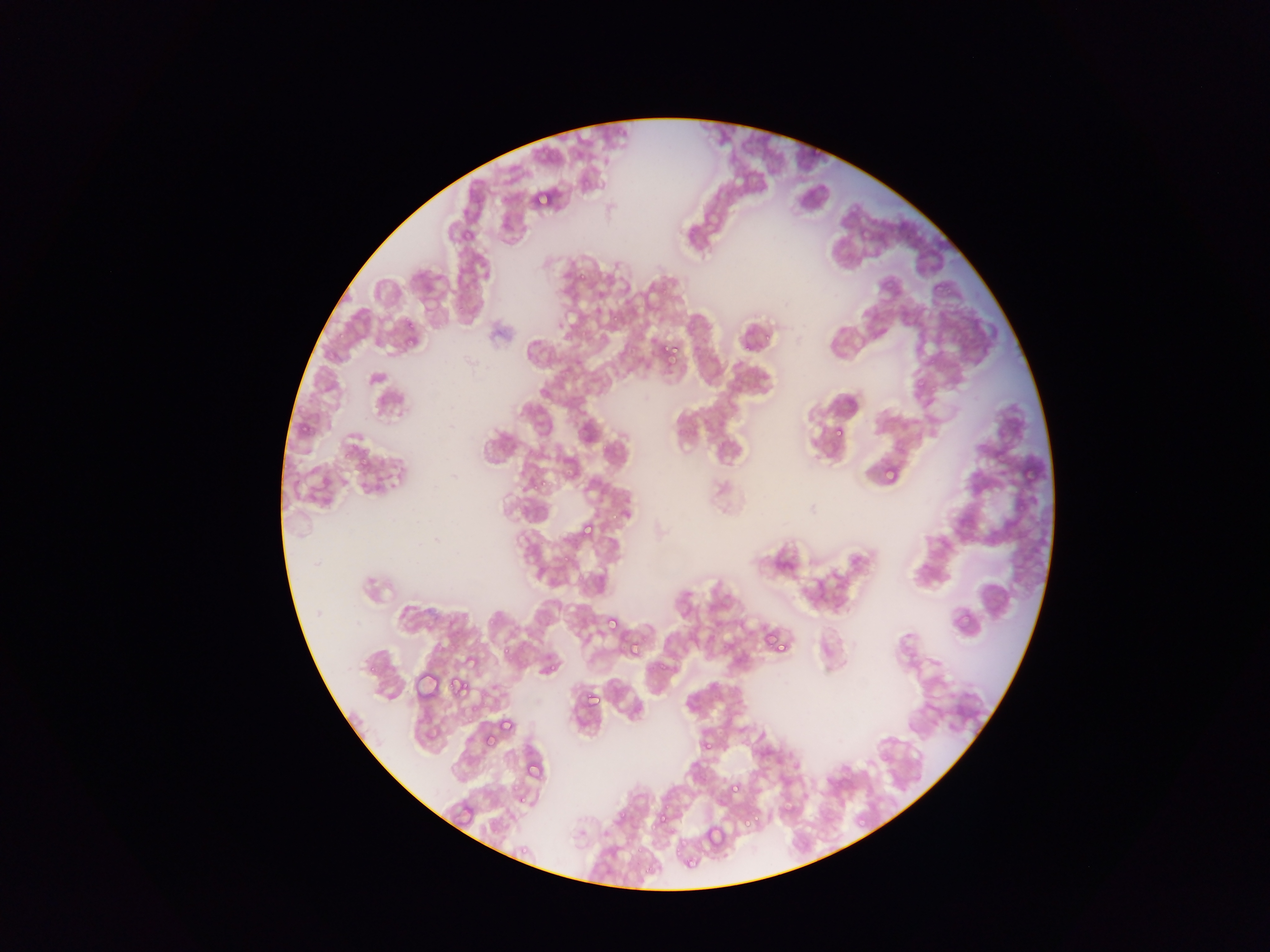

Approximate bounding boxes as [left, top, right, bottom] in pixels.
Summary:
  - Plasmodium parasite locations: [533, 186, 554, 204], [933, 282, 943, 292], [899, 307, 909, 318], [404, 320, 414, 331], [335, 330, 344, 340], [660, 343, 676, 359], [926, 354, 938, 366], [914, 377, 926, 391], [296, 422, 315, 439], [833, 425, 844, 436], [996, 438, 1011, 454], [993, 446, 1009, 462], [1020, 463, 1035, 479], [882, 464, 899, 483], [539, 474, 557, 489], [601, 507, 621, 524], [579, 522, 596, 540], [559, 552, 576, 566], [952, 609, 972, 630], [605, 615, 620, 630], [765, 628, 784, 649], [761, 629, 776, 646], [494, 634, 516, 657], [624, 641, 646, 659], [538, 660, 557, 674], [412, 674, 442, 699], [449, 677, 467, 696], [583, 690, 600, 707], [502, 715, 517, 735], [482, 732, 495, 745], [700, 740, 713, 752], [702, 742, 717, 755], [527, 764, 544, 781], [726, 778, 747, 796], [512, 789, 522, 808], [651, 804, 683, 827], [740, 814, 757, 831], [855, 815, 866, 826], [704, 823, 724, 846], [671, 840, 695, 850], [515, 843, 533, 855], [676, 861, 707, 874]
  - Capture: mobile-phone photograph through a microscope
  - Image size: 1270×952 pixels
  - Preparation: thin blood film
  - Country: Ghana
  - Field of view: single